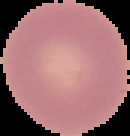
result = no malaria parasites seen
image type = cell region segmented out of the field of view; surrounding area masked to black
image size = 130×136 pixels
preparation = thin blood smear